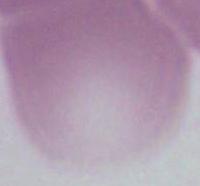
Photomicrograph. A red blood cell is seen. 1000x magnification.